Give the extent of all uninfected red blood cells.
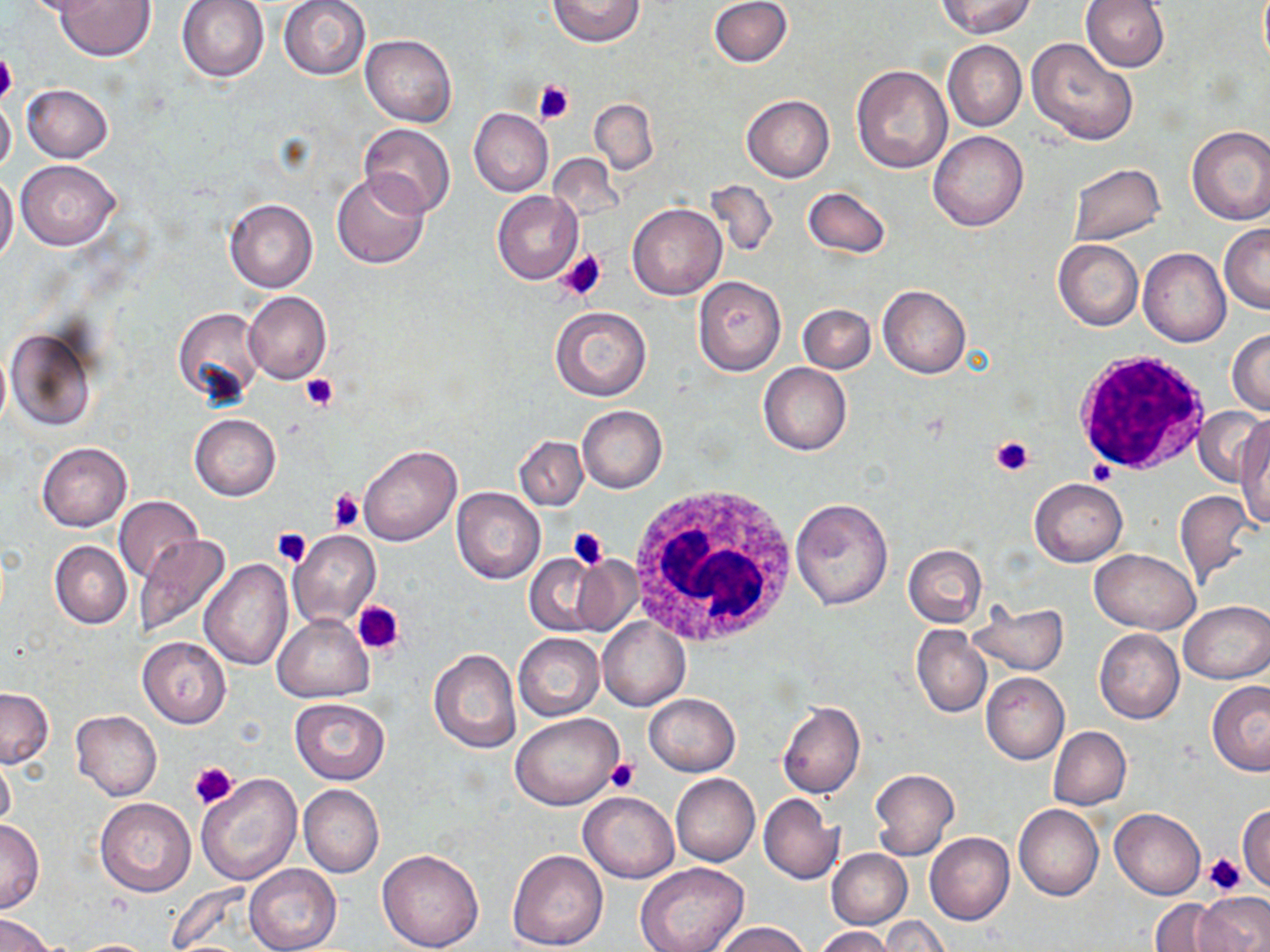

Approximate bounding boxes as (x1,y1)-(x2,y2) corner pairs in pixels.
Uninfected red blood cells: (23,0)-(114,19), (53,0)-(156,59), (178,0)-(270,81), (278,0)-(371,80), (548,0)-(644,47), (709,0)-(792,67), (936,0)-(1035,37), (1081,0)-(1170,71), (361,34)-(456,127), (1027,37)-(1138,145), (943,39)-(1027,131), (851,66)-(951,174), (22,84)-(113,162), (742,95)-(834,182), (0,96)-(16,177), (589,99)-(658,174), (469,108)-(553,196), (359,123)-(456,217), (1185,125)-(1270,225), (929,131)-(1028,231), (15,160)-(120,249), (1067,164)-(1166,246), (332,172)-(429,268), (0,173)-(18,266), (705,179)-(779,259), (802,186)-(891,258), (493,190)-(582,284), (225,199)-(318,293), (627,203)-(726,300), (1219,224)-(1270,313), (1053,239)-(1143,330), (1138,247)-(1230,347), (692,275)-(786,376), (878,284)-(970,377), (244,290)-(331,384), (798,304)-(875,373), (549,305)-(652,401), (172,306)-(266,409), (6,328)-(97,431), (1227,329)-(1270,415), (758,363)-(851,455), (577,405)-(667,492), (1193,408)-(1268,486), (190,414)-(281,500), (1237,423)-(1270,529), (513,435)-(587,510), (36,442)-(132,532), (358,444)-(461,546), (1030,478)-(1127,566), (451,487)-(545,584), (1174,490)-(1256,585), (115,496)-(203,583), (790,497)-(894,611), (289,530)-(381,629), (133,535)-(234,636), (50,541)-(132,629), (902,544)-(988,627), (1091,550)-(1199,633), (524,553)-(613,638), (564,554)-(644,636), (200,560)-(293,668), (1179,599)-(1270,683), (969,602)-(1068,676), (274,614)-(373,702), (597,617)-(690,711), (911,625)-(991,717), (1095,628)-(1184,724), (514,633)-(604,721), (137,636)-(232,727), (428,649)-(521,754), (980,673)-(1070,764), (1207,681)-(1270,775), (0,687)-(53,767), (645,694)-(740,776), (290,697)-(390,784), (778,701)-(865,799), (71,710)-(162,801), (511,712)-(623,810), (1049,726)-(1131,809), (0,754)-(15,830), (870,768)-(959,859), (195,771)-(302,886), (671,773)-(760,866), (298,784)-(383,878), (579,791)-(679,883), (758,794)-(844,885), (96,798)-(196,896), (1237,802)-(1270,890), (1013,804)-(1103,900), (1109,808)-(1205,899), (0,818)-(44,913), (925,832)-(1015,925), (376,849)-(485,951), (506,849)-(609,950), (827,849)-(911,928), (635,864)-(750,952), (244,865)-(340,952), (1196,892)-(1269,952), (1151,898)-(1235,951), (0,913)-(56,951), (878,917)-(951,951), (715,922)-(810,952), (815,927)-(896,952), (68,939)-(161,952).

Summary:
  - White blood cell locations: (1073,350)-(1213,474), (628,488)-(800,650)
  - Platelet locations: (0,49)-(17,107), (532,78)-(575,125), (556,249)-(608,301), (301,374)-(339,411), (990,434)-(1035,476), (1088,458)-(1117,485), (327,488)-(365,531), (271,526)-(312,567), (567,527)-(608,571), (353,602)-(404,656), (607,756)-(639,793), (190,761)-(239,808), (1203,852)-(1247,896)
  - Slide-level diagnosis: negative for blood parasites
  - Preparation: thin blood film
  - Field of view: single
  - Image size: 1270×952 pixels
  - Stain: May-Grünwald-Giemsa
  - Modality: light microscopy
  - Magnification: 1000x